Report the malaria status of this cell.
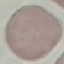

Uninfected.

preparation = thin blood film
capture = smartphone camera at the microscope eyepiece
stain = Giemsa
image type = cell patch, automatically extracted from a larger field of view and resized to 64 × 64 pixels